Point out each malaria parasite.
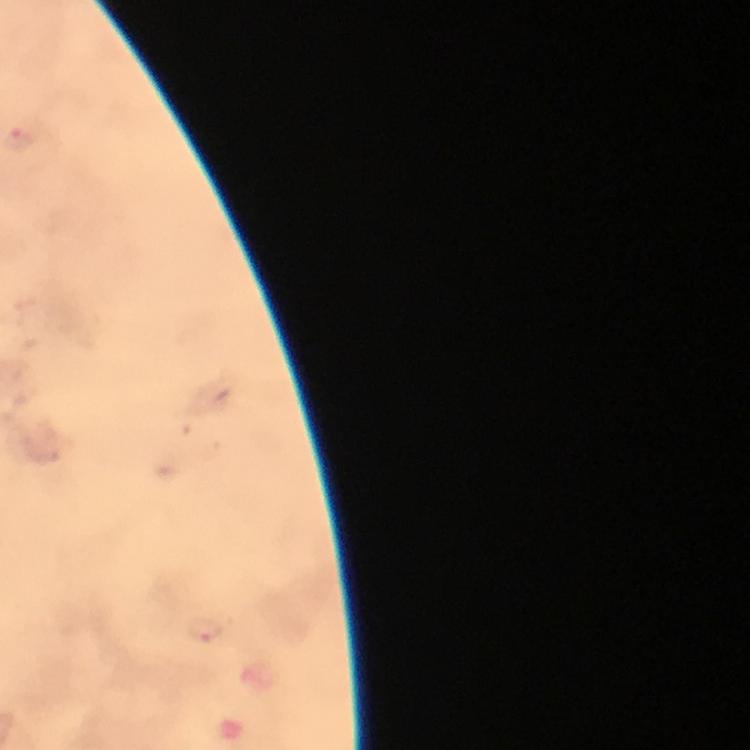
Approximate centers as [x, y] in pixels.
Malaria parasites: [206, 632].

Summary:
  - Magnification: 100x
  - Context: from a diagnostic examination for malaria
  - Capture: smartphone mounted on the microscope
  - Image size: 750×750 pixels
  - Cropped from: one field of view
  - Preparation: thick smear
  - Immersion oil: used
  - Stain: Giemsa